Assess the morphology of the erythrocytes.
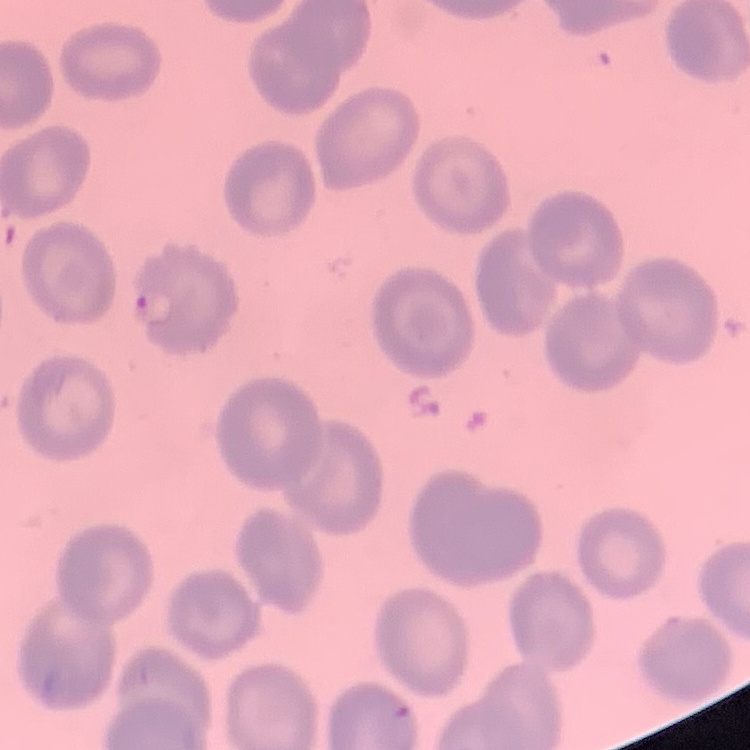
They show no rouleaux formation.

Field's or Giemsa stain. Thin blood smear. One tile cut from a larger photomicrograph.